Locate every Plasmodium ovale-infected red blood cell.
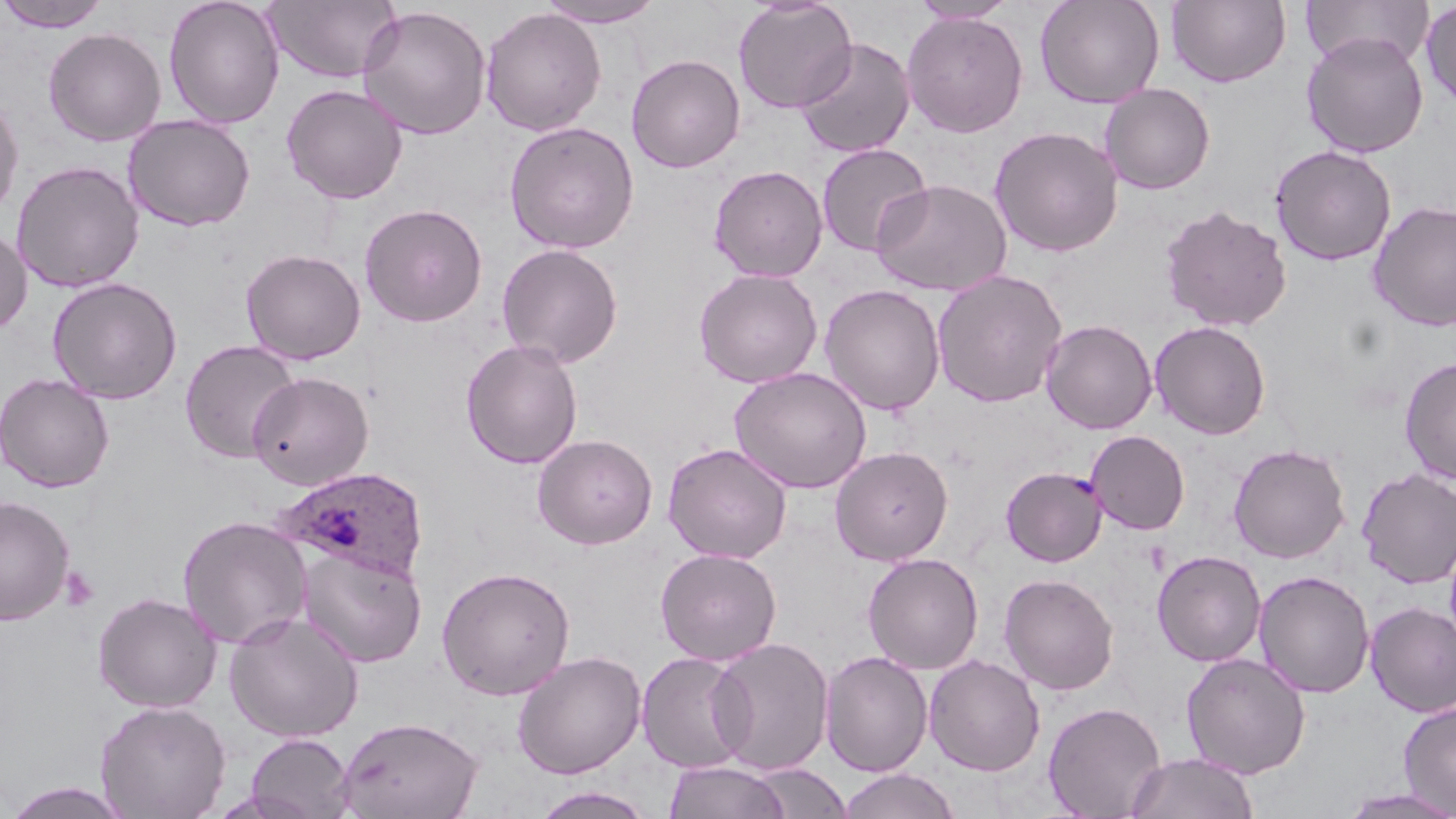

Approximate bounding boxes as (x1,y1)-(x2,y2) corner pairs in pixels.
Plasmodium ovale-infected red blood cells: (275,466)-(430,583).

Summary:
  - Platelet locations: (60,566)-(100,612)
  - Uninfected red blood cell locations: (0,0)-(113,32), (163,0)-(285,129), (264,0)-(401,84), (535,0)-(666,28), (732,0)-(857,113), (1034,0)-(1165,109), (1166,0)-(1291,88), (1301,0)-(1435,69), (908,1)-(1020,24), (1420,2)-(1456,110), (357,5)-(492,140), (480,7)-(606,136), (901,11)-(1028,137), (43,27)-(166,146), (1301,31)-(1429,158), (795,38)-(915,158), (626,54)-(745,173), (281,83)-(407,204), (1099,83)-(1215,195), (0,93)-(24,223), (123,115)-(256,232), (504,121)-(640,254), (989,125)-(1124,257), (816,143)-(933,257), (1269,144)-(1397,266), (11,160)-(145,293), (708,165)-(828,282), (872,178)-(1012,296), (1367,200)-(1456,331), (359,203)-(488,327), (1159,205)-(1293,332), (0,226)-(32,335), (497,243)-(623,367), (241,248)-(366,365), (694,268)-(823,388), (932,269)-(1068,408), (46,276)-(183,404), (820,284)-(945,416), (1040,319)-(1157,434), (1150,320)-(1271,439), (179,339)-(301,463), (461,339)-(583,469), (1399,357)-(1456,485), (729,367)-(871,494), (247,371)-(374,490), (0,372)-(115,493), (1086,430)-(1190,535), (533,433)-(658,549), (662,442)-(792,563), (1228,443)-(1350,563), (830,447)-(953,566), (1000,466)-(1106,566), (1356,467)-(1456,589), (0,495)-(75,625), (177,514)-(312,649), (296,546)-(427,667), (655,548)-(782,665), (1152,549)-(1267,667), (862,552)-(984,674), (436,566)-(575,700), (1254,570)-(1375,699), (999,573)-(1119,695), (93,592)-(222,712), (1365,601)-(1456,717), (223,611)-(365,743), (709,637)-(835,774), (511,650)-(646,779), (820,650)-(933,776), (636,652)-(753,773), (1181,652)-(1310,779), (924,654)-(1046,776), (95,700)-(231,819), (1397,700)-(1456,816), (1042,701)-(1167,818), (336,716)-(485,819), (245,733)-(356,818), (1125,752)-(1260,819), (663,760)-(791,819), (748,763)-(852,818), (836,768)-(961,819), (2,781)-(136,818), (532,785)-(657,819), (1337,788)-(1456,819)
  - Slide-level diagnosis: Plasmodium ovale
  - Magnification: 1000x
  - Stain: May-Grünwald-Giemsa
  - Image size: 1456×819 pixels
  - Field of view: single
  - Preparation: thin blood smear
  - Modality: light microscopy